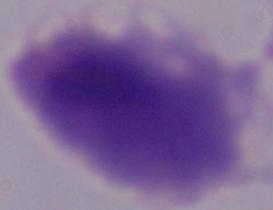
A trichomonad is shown. Photomicrograph. Captured at 1000x magnification.